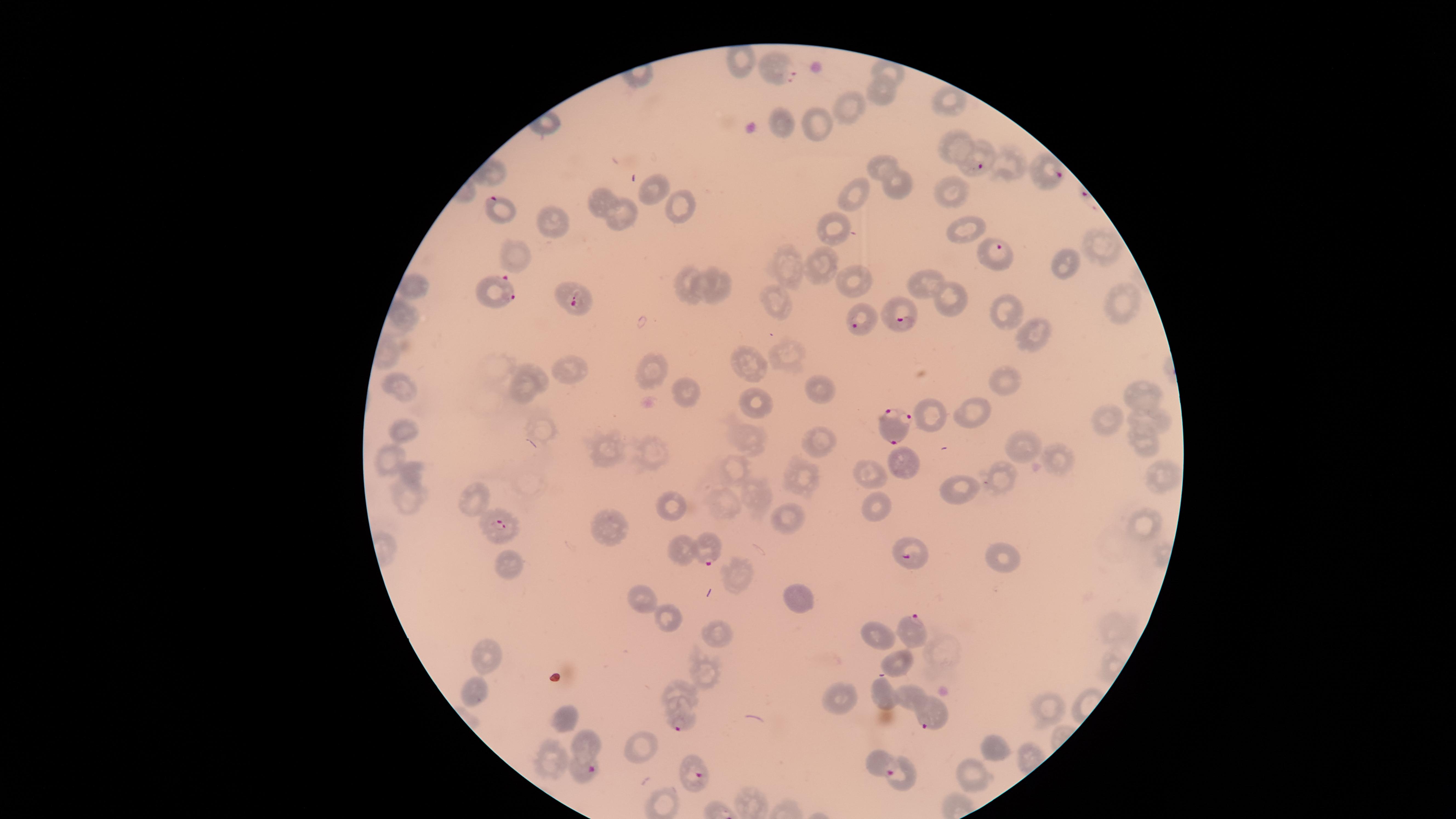

Approximate marker points as [x, y] in pixels.
Summary:
  - Uninfected RBCs: [892, 71], [884, 93], [949, 102], [849, 104], [784, 124], [822, 127], [955, 144], [879, 165], [1010, 166], [896, 185], [651, 188], [851, 194], [954, 198], [601, 203], [683, 206], [618, 216], [552, 223], [964, 227], [837, 234], [1100, 249], [507, 256], [1059, 260], [822, 264], [791, 267], [853, 279], [713, 281], [690, 285], [922, 285], [416, 291], [1110, 292], [955, 300], [776, 303], [1006, 313], [401, 315], [1025, 334], [788, 357], [651, 368], [566, 369], [753, 371], [1006, 382], [526, 386], [816, 389], [402, 390], [684, 393], [1142, 393], [752, 407], [977, 408], [932, 417], [1106, 422], [1151, 422], [405, 426], [824, 439], [753, 440], [1143, 444], [1022, 447], [652, 451], [611, 452], [388, 457], [1063, 462], [909, 463], [870, 467], [735, 468], [414, 473], [1157, 473], [805, 477], [1004, 479], [756, 492], [960, 492], [475, 496], [410, 497], [728, 505], [676, 506], [873, 511], [788, 519], [609, 525], [1149, 527], [681, 550], [999, 560], [512, 568], [741, 577], [643, 598], [801, 602], [661, 614], [722, 635], [876, 642], [488, 657], [903, 661], [707, 670], [476, 685], [682, 689], [883, 693], [909, 697], [843, 701], [1050, 710], [564, 715], [589, 743], [643, 745], [995, 746], [557, 757], [877, 759], [968, 776]
  - Parasitized RBCs: [777, 68], [982, 165], [1053, 175], [506, 212], [999, 250], [499, 298], [570, 302], [899, 320], [856, 321], [894, 426], [493, 525], [706, 556], [907, 561], [911, 625], [929, 717], [679, 723], [589, 773], [902, 775], [697, 779]
  - Visible region: circular
  - Preparation: thin blood film
  - Species: Plasmodium falciparum
  - Image size: 1456×819 pixels
  - Field of view: single
  - Stain: Giemsa
  - Presence: malaria parasites seen
  - Capture: smartphone photograph through the microscope eyepiece